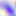 Captured at 400x magnification. Photomicrograph. Toxoplasma gondii is seen.